Classify this cell by malaria status.
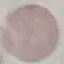

Uninfected.

Summary:
  - Capture: smartphone through the microscope eyepiece
  - Stain: Giemsa
  - Image type: automatically extracted cell patch, resized to 64 × 64 pixels
  - Preparation: thin blood smear